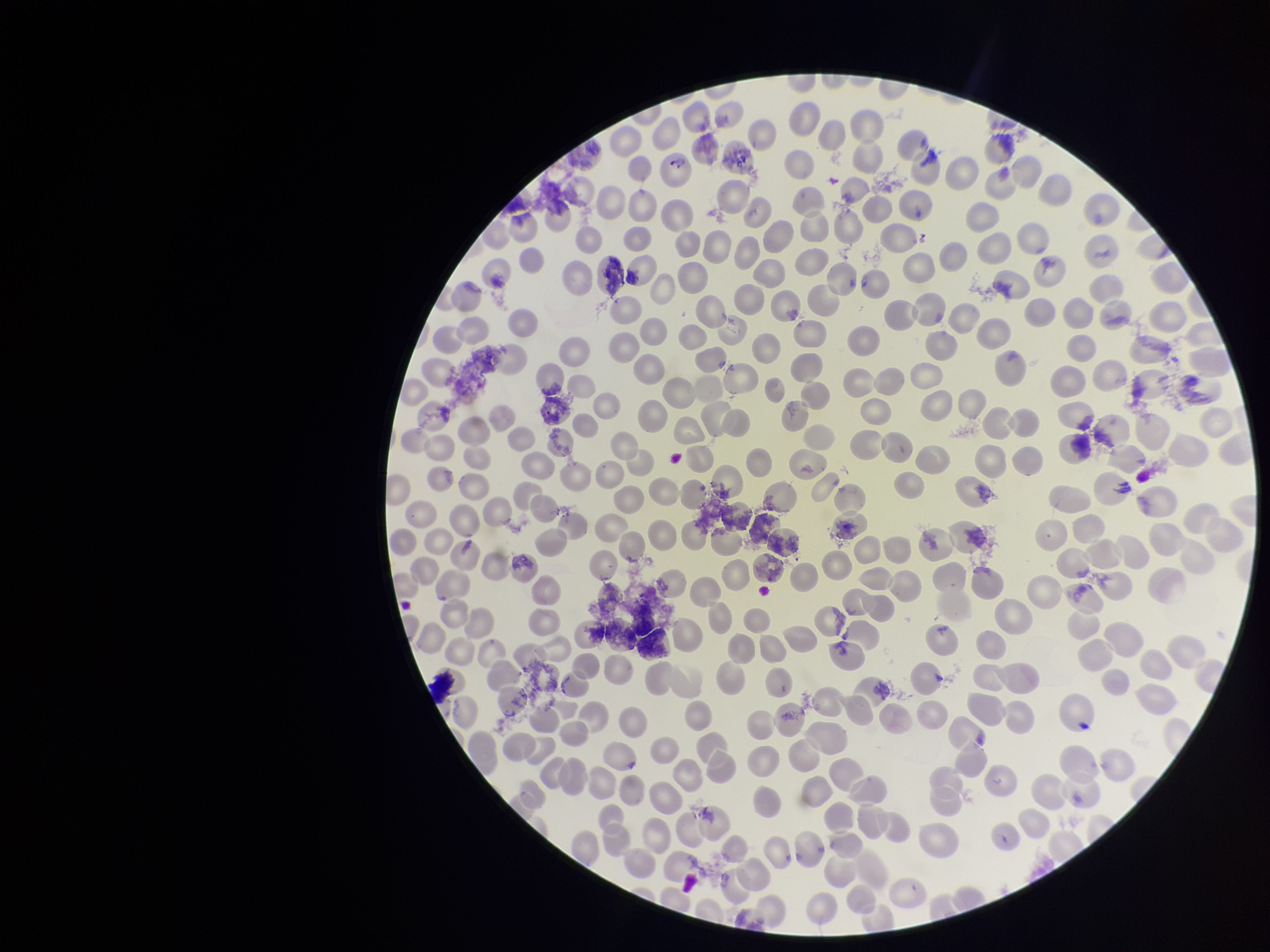

Single field of view. Parasitized red blood cells: none detected. Patient malaria status: positive. Smartphone photograph taken through the eyepiece of a microscope. Species reported for this patient: Plasmodium vivax. Preparation: thin blood smear. Parasitized red blood cell count: 0. Red blood cell count: 300. Image is 1270×952 pixels. Stained with Giemsa.